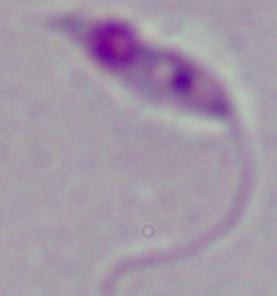
A Leishmania parasite is shown. Micrograph. Captured at 1000x magnification.